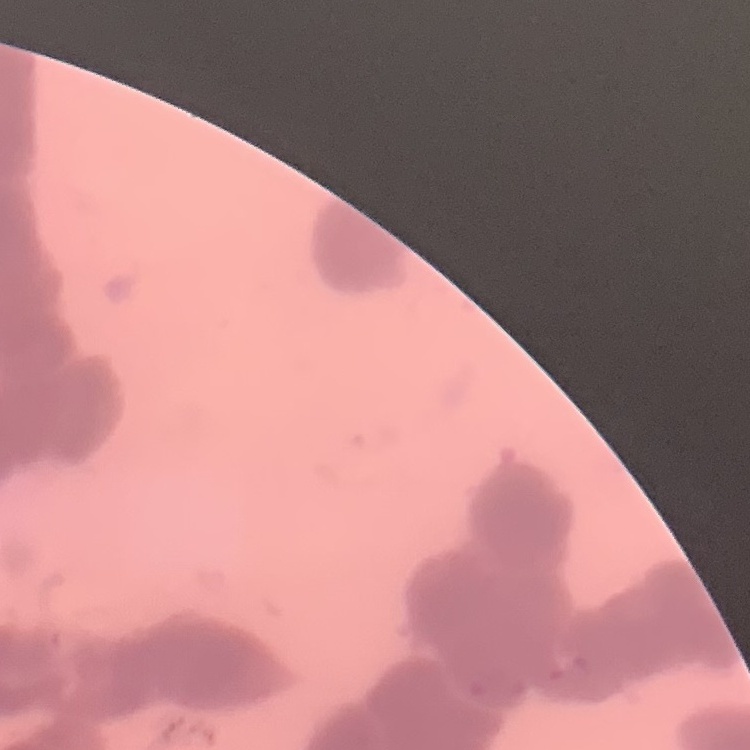
{
  "red_blood_cell_morphology": "rouleaux formation",
  "stain": "Field's or Giemsa",
  "image_type": "square crop of a larger photomicrograph",
  "preparation": "thin peripheral smear"
}